Give the extent of all uninfected red blood cells.
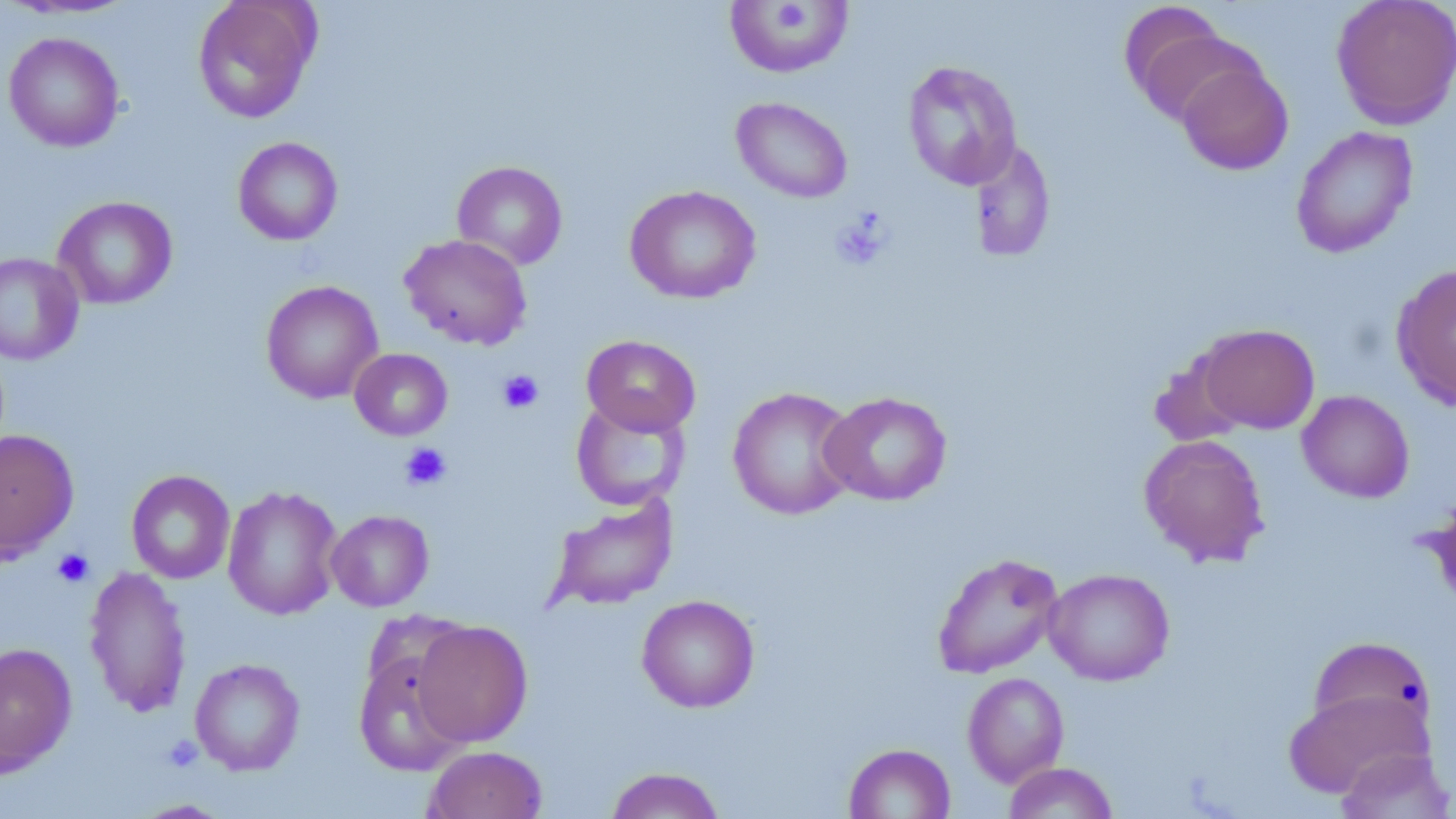

Approximate bounding boxes as (x1,y1)-(x2,y2) corner pairs in pixels.
Uninfected red blood cells: (192,0)-(321,123), (1331,0)-(1456,129), (724,2)-(854,78), (1121,7)-(1251,126), (3,32)-(124,152), (901,59)-(1023,190), (1176,59)-(1294,175), (731,97)-(853,203), (1290,125)-(1419,259), (233,136)-(343,245), (971,140)-(1057,263), (452,160)-(568,270), (624,185)-(762,305), (53,196)-(178,309), (399,234)-(532,350), (0,252)-(84,365), (1390,262)-(1456,411), (260,280)-(383,404), (1195,323)-(1320,434), (581,334)-(701,436), (349,348)-(453,441), (727,387)-(860,520), (1296,389)-(1414,502), (819,391)-(953,507), (571,398)-(690,510), (0,429)-(79,561), (1139,433)-(1270,567), (126,470)-(235,584), (222,484)-(343,620), (1423,493)-(1456,616), (546,494)-(678,611), (326,509)-(434,612), (931,551)-(1065,679), (83,565)-(193,718), (1044,568)-(1175,686), (637,594)-(760,713), (411,620)-(533,747), (1307,636)-(1436,740), (0,642)-(77,777), (353,649)-(470,777), (190,658)-(305,775), (962,672)-(1069,787), (1284,688)-(1432,798), (843,743)-(955,819), (424,745)-(547,819), (1335,746)-(1453,819), (1003,762)-(1119,819), (604,766)-(727,818), (131,799)-(235,818).

Platelet locations: (773,3)-(814,31), (829,209)-(893,271), (497,369)-(544,414), (400,442)-(452,491), (52,548)-(95,588), (161,735)-(203,771). Slide-level diagnosis: negative for blood parasites. Light microscopy. Image is 1456×819 pixels. May-Grünwald-Giemsa-stained preparation. Thin blood film. One field of a larger specimen. 1000x magnification.